Classify this cell by malaria status.
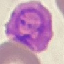

It is parasitized.

preparation = thin blood smear
capture = smartphone through the microscope eyepiece
stain = Giemsa
image type = automatically extracted cell patch, resized to 64 × 64 pixels